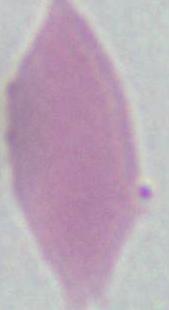

magnification = 1000x
modality = micrograph
identification = red blood cell